Assess the morphology of the erythrocytes.
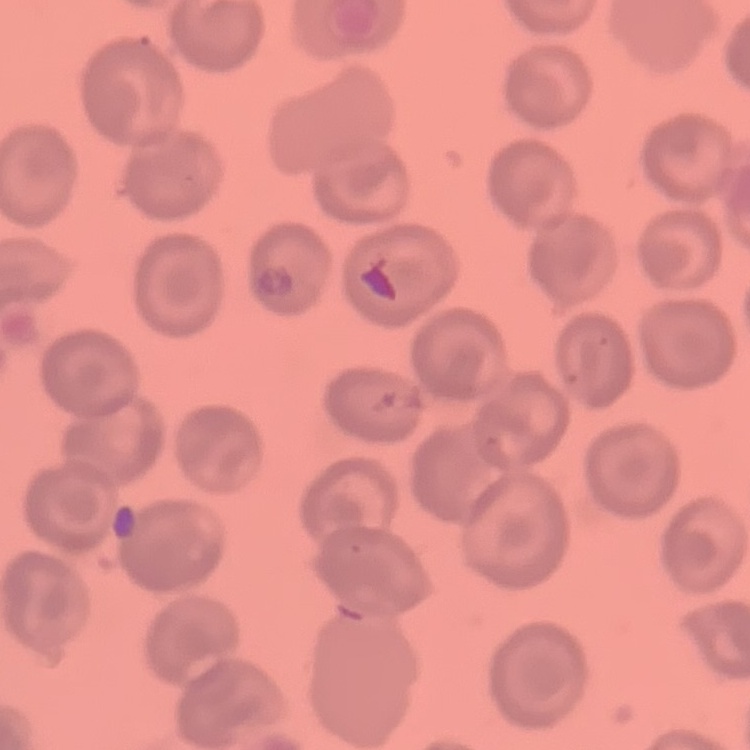
No rouleaux formation.

Stained with either Field's or Giemsa. Thin blood film. One tile cut from a larger photomicrograph.